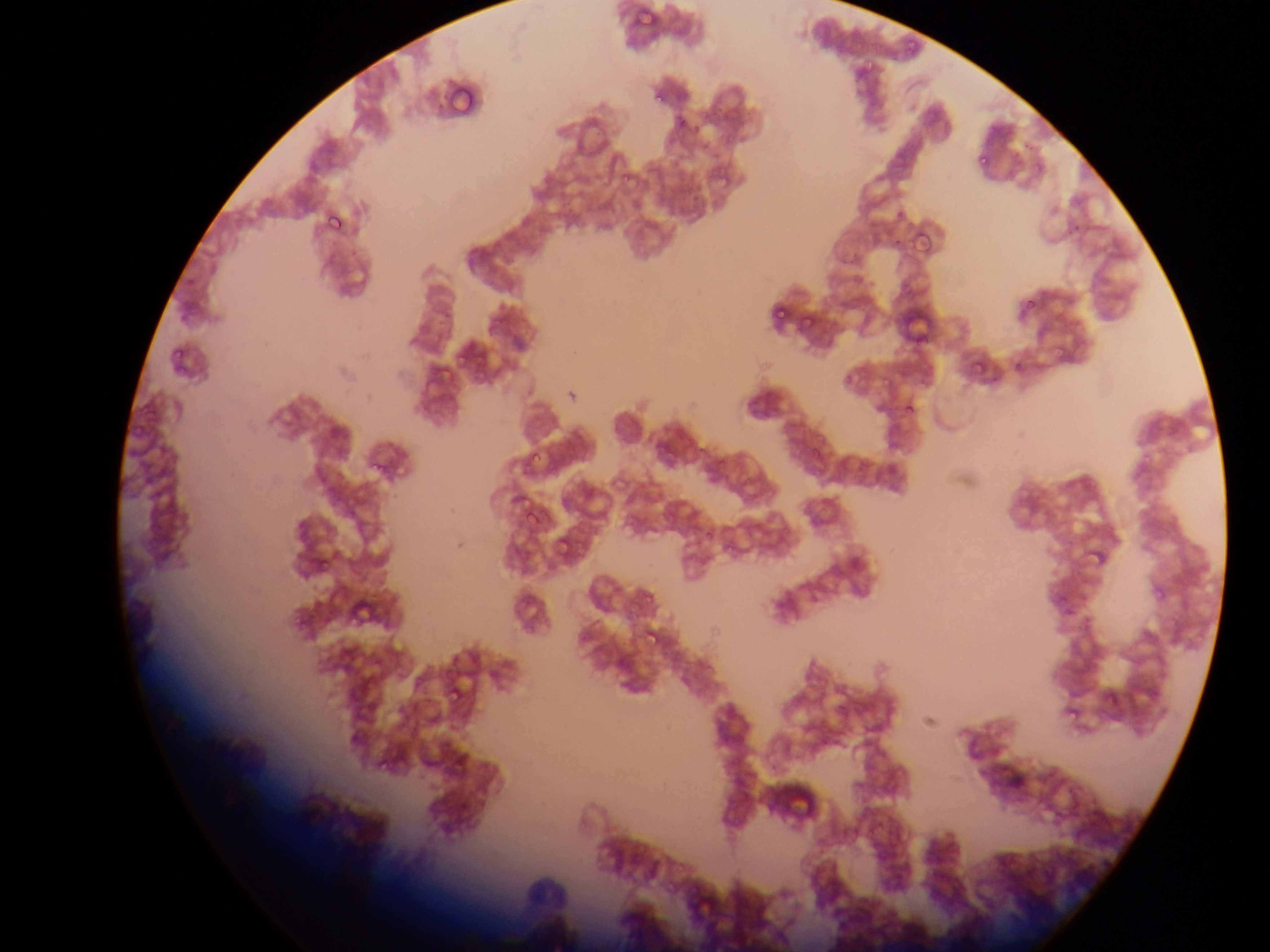

Approximate bounding boxes as {left, top, right, bottom} in pixels.
Summary:
  - Malaria parasite locations: {632, 4, 660, 33}, {904, 39, 920, 54}, {860, 50, 877, 80}, {652, 84, 669, 104}, {973, 148, 990, 166}, {613, 160, 630, 181}, {321, 207, 353, 240}, {910, 231, 928, 253}, {771, 296, 794, 321}, {1023, 298, 1038, 314}, {801, 314, 817, 333}, {968, 353, 989, 375}, {454, 356, 467, 373}, {473, 373, 491, 390}, {902, 398, 921, 419}, {525, 442, 545, 466}, {368, 461, 384, 475}, {522, 519, 534, 526}, {554, 533, 578, 561}, {1084, 539, 1102, 564}, {312, 553, 334, 570}, {643, 626, 665, 651}, {442, 681, 466, 708}, {1060, 708, 1077, 729}
  - Leukocyte locations: {768, 775, 828, 833}
  - Field of view: single
  - Preparation: thin blood smear
  - Country: Ghana
  - Capture: mobile-phone photograph through a microscope
  - Image size: 1270×952 pixels